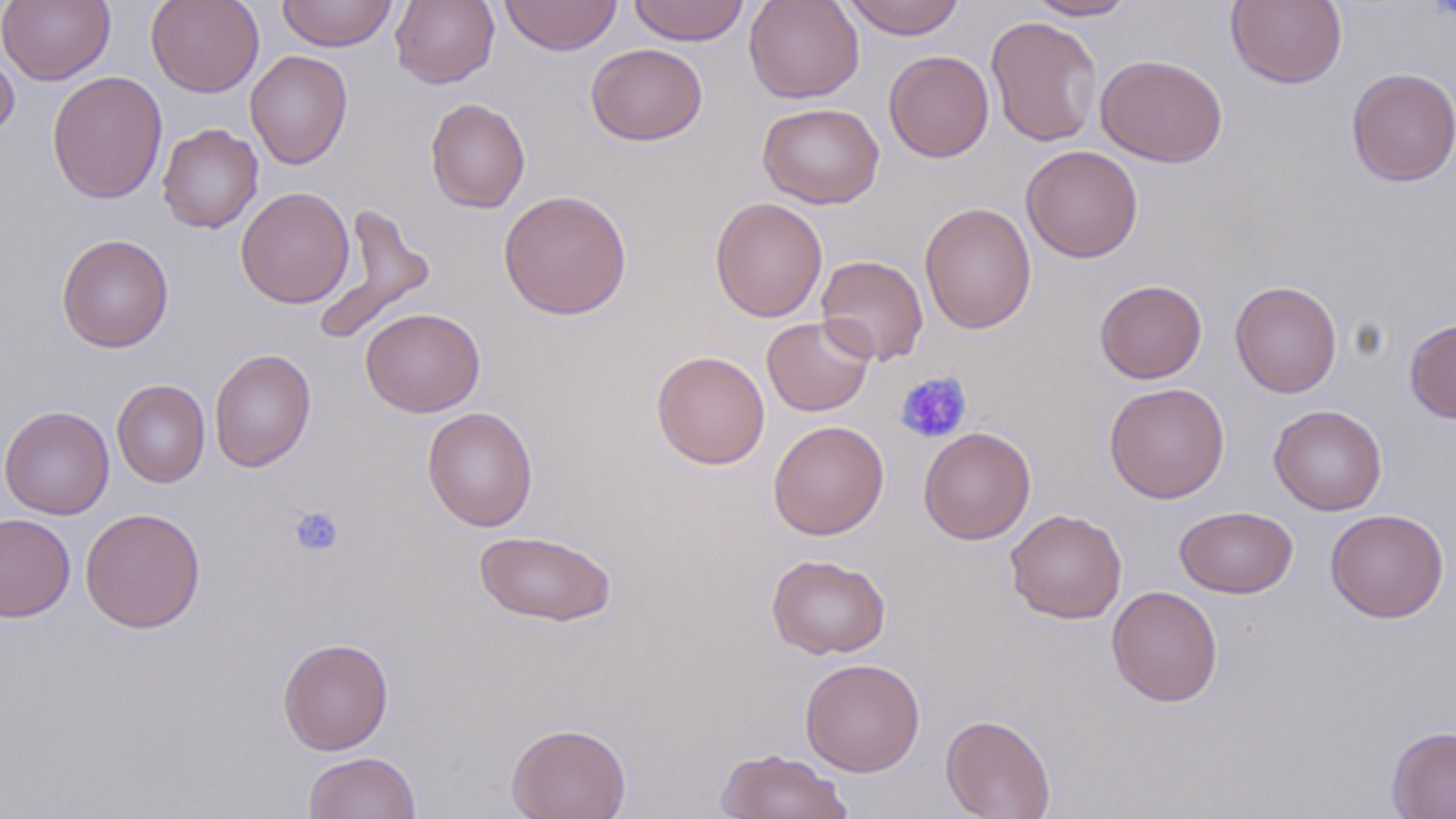
Approximate bounding boxes as (x1,y1)-(x2,y2) corner pairs in pixels. Platelet locations: (895,371)-(972,444), (289,506)-(344,557). Uninfected red blood cell locations: (0,0)-(115,85), (146,0)-(264,97), (276,0)-(397,52), (390,0)-(499,89), (499,0)-(622,55), (628,0)-(749,45), (744,0)-(865,103), (840,0)-(966,39), (1226,0)-(1347,89), (1024,1)-(1136,21), (986,15)-(1103,148), (586,43)-(707,146), (0,45)-(19,143), (245,50)-(353,170), (883,50)-(995,162), (1096,54)-(1228,167), (1346,67)-(1456,186), (47,71)-(167,204), (425,98)-(530,213), (757,102)-(884,209), (157,123)-(264,233), (1021,144)-(1143,263), (236,186)-(355,309), (498,189)-(632,320), (710,196)-(828,322), (919,201)-(1037,334), (312,203)-(435,344), (56,233)-(174,352), (815,254)-(929,366), (1095,279)-(1207,384), (1229,280)-(1343,398), (361,307)-(485,417), (761,315)-(875,417), (1405,317)-(1456,424), (209,348)-(316,473), (651,350)-(770,469), (112,379)-(210,487), (1104,382)-(1230,504), (1269,404)-(1387,515), (0,405)-(115,519), (423,407)-(538,531), (768,420)-(889,539), (918,427)-(1036,544), (1175,506)-(1298,599), (80,508)-(206,633), (1005,508)-(1127,624), (1325,508)-(1449,623), (0,514)-(75,622), (473,530)-(616,628), (766,554)-(891,659), (1106,585)-(1223,706), (278,637)-(393,755), (800,658)-(925,776), (941,714)-(1056,819), (506,722)-(631,819), (1387,726)-(1456,818), (716,748)-(854,819), (304,751)-(420,818). Slide-level diagnosis: no evidence of blood parasites. Single field of view. 1000x magnification. Thin blood film. Optical microscopy. May-Grünwald-Giemsa-stained preparation. Image is 1456×819 pixels.